Identify the parasite.
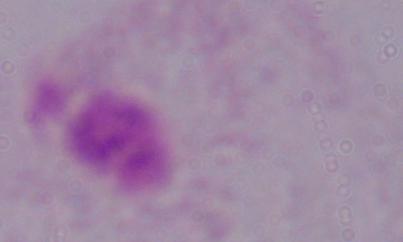
A trichomonad.

Captured at 1000x magnification. Micrograph.